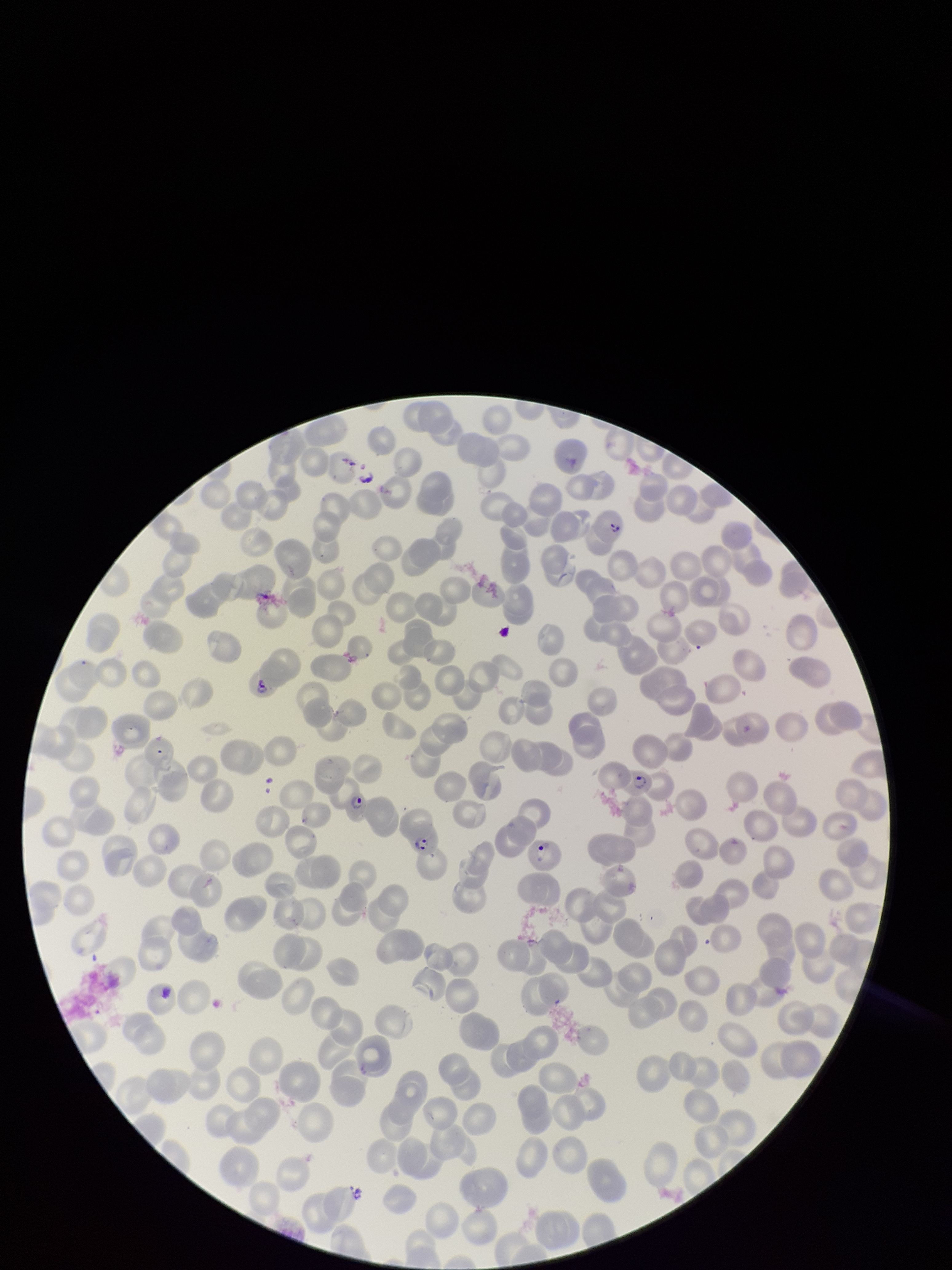 Stained with Giemsa. Parasitized red blood cells: detected. Preparation: thin blood smear. Parasitized red blood cell count: 7. Image is 952×1270 pixels. Single field of view. Red blood cell count: 222. Smartphone photograph taken through the eyepiece of a microscope. Species reported for this patient: Plasmodium falciparum. Patient malaria status: infected.